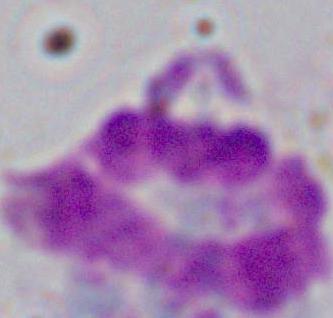

Summary:
  - Modality: photomicrograph
  - Magnification: 1000x
  - Identification: white blood cell